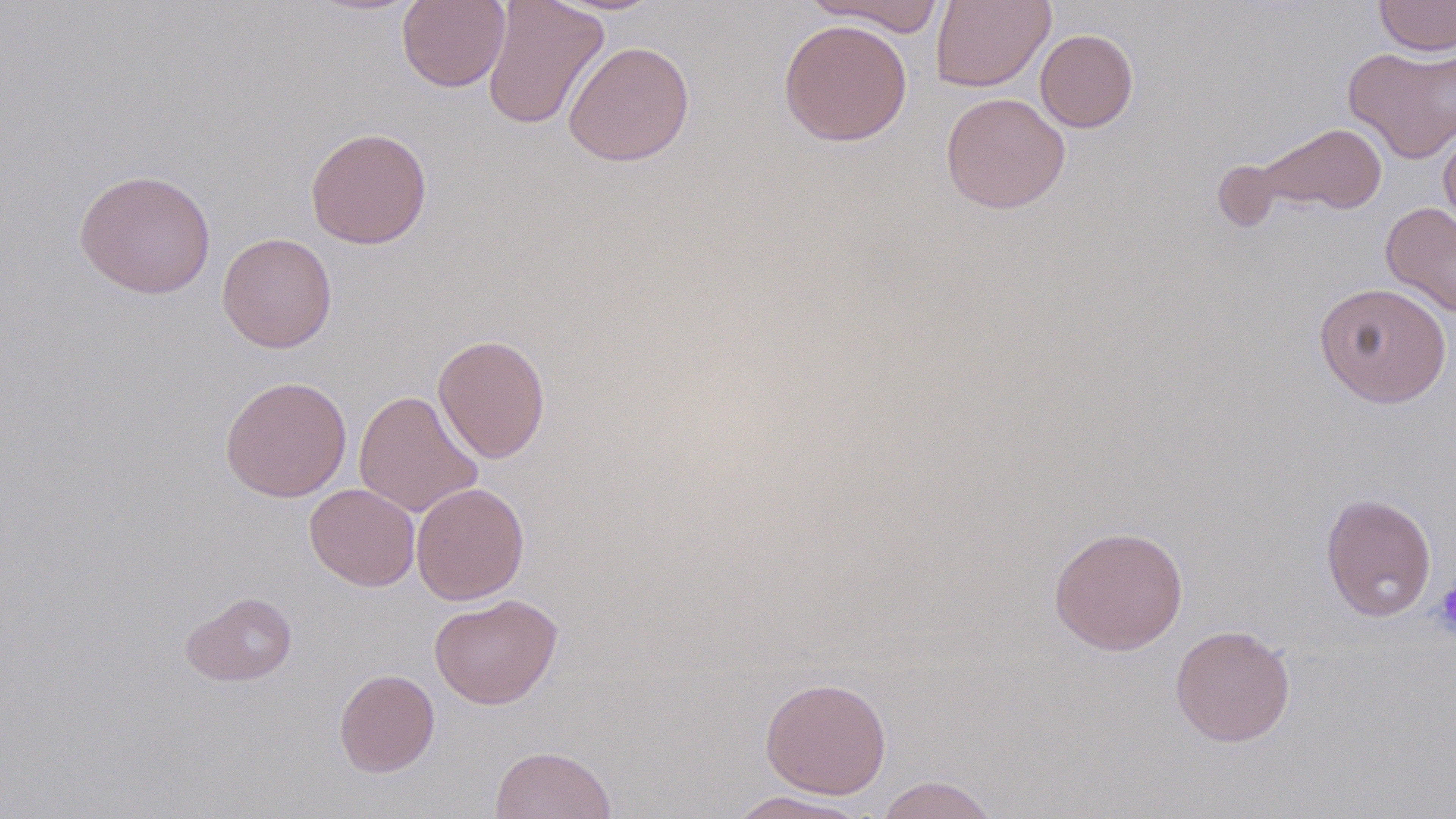
Approximate bounding boxes as (x1,y1)-(x2,y2) corner pairs in pixels. Platelet locations: (1432,580)-(1456,640). Uninfected red blood cell locations: (482,0)-(609,131), (802,0)-(947,36), (931,0)-(1055,92), (1373,0)-(1456,57), (396,1)-(510,92), (778,18)-(913,146), (1035,28)-(1138,132), (563,40)-(695,166), (1343,43)-(1456,163), (940,93)-(1070,213), (1255,122)-(1388,216), (1439,126)-(1456,233), (305,127)-(433,250), (74,168)-(216,299), (1380,201)-(1456,319), (216,232)-(337,352), (1313,281)-(1452,407), (433,333)-(551,463), (220,375)-(352,502), (353,390)-(483,518), (411,482)-(529,605), (305,483)-(420,591), (1320,493)-(1437,622), (1048,525)-(1188,655), (181,591)-(298,686), (429,593)-(563,710), (1170,624)-(1296,747), (334,669)-(439,777), (760,677)-(891,799), (490,745)-(616,819), (875,775)-(1000,819), (724,791)-(873,818). Slide-level diagnosis: negative for blood parasites. 1000x magnification. Image is 1456×819 pixels. Optical microscopy. Thin blood film. Single field of view. May-Grünwald-Giemsa-stained preparation.